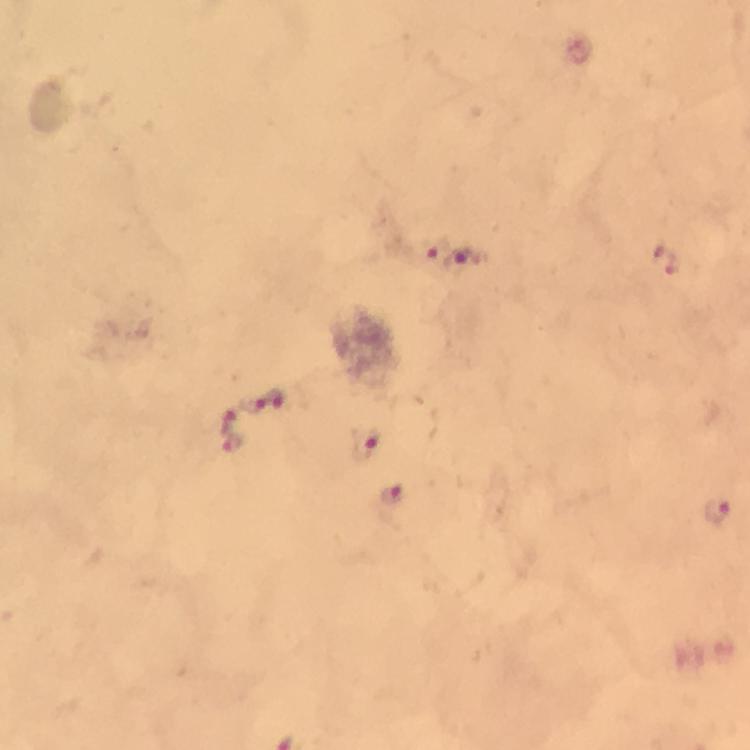 Approximate centers as [x, y] in pixels. Malaria parasite locations: [432, 253], [669, 259], [461, 262], [278, 399], [254, 404], [225, 417], [233, 441], [365, 444], [391, 496], [716, 509]. Giemsa stain. From a malaria diagnostic workup. Immersion oil was used. Photographed through the microscope with a smartphone camera. 100x magnification. Thick blood film. Cropped region of a single field of view. Image is 750×750 pixels.